Name the parasite shown.
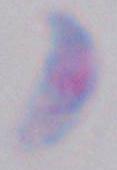

Toxoplasma gondii.

Photomicrograph. Captured at 1000x magnification.